Look for Plasmodium parasites.
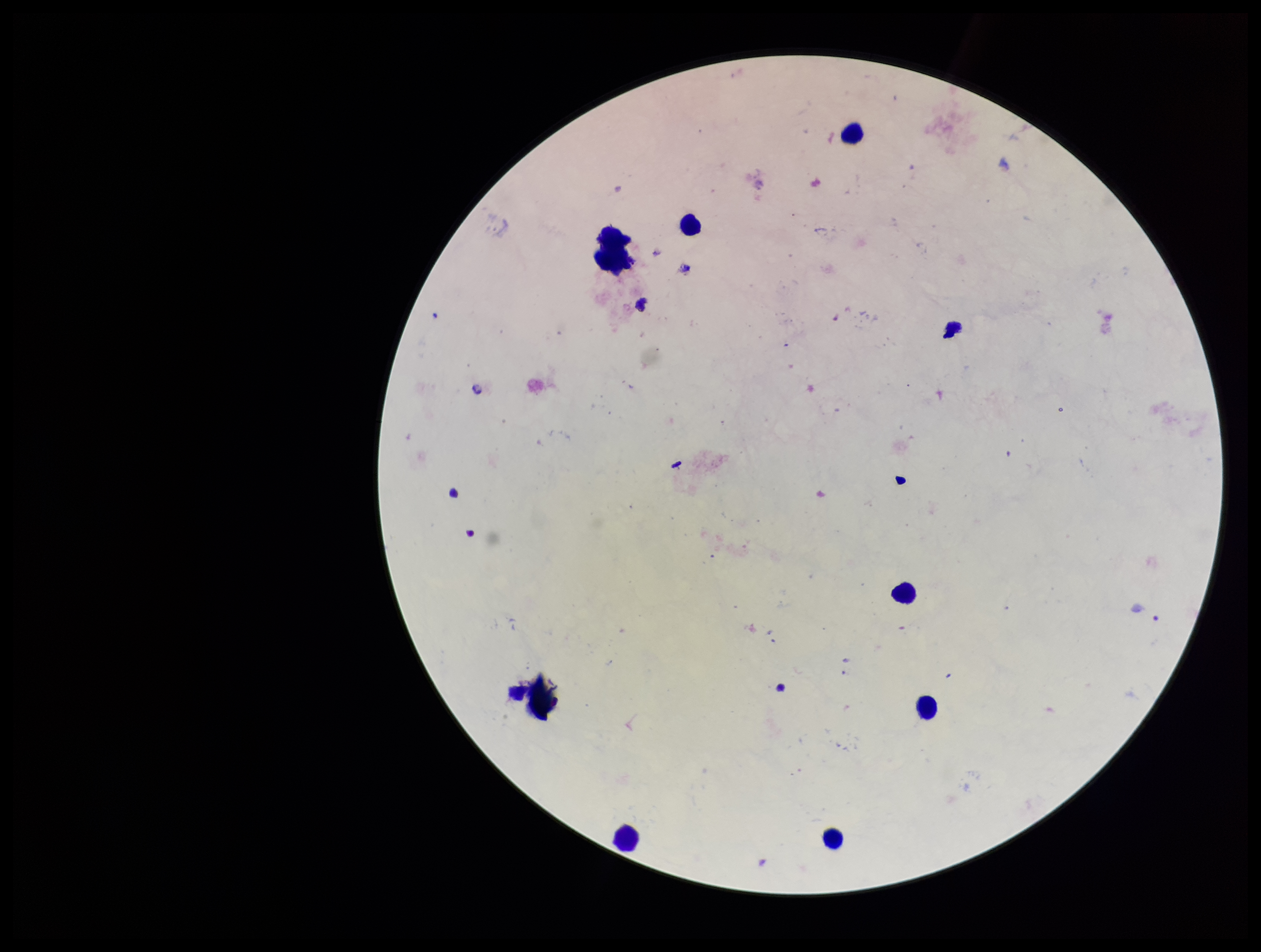

None detected.

image_size: 1261×952 pixels
leukocyte_count: 6
parasite_count: 0
field_of_view: one from this slide
patient_malaria_status: negative
capture: smartphone photograph through the microscope eyepiece
stain: Giemsa
preparation: thick smear